State which parasite is depicted.
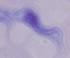

This is a trypanosome.

Summary:
  - Magnification: 1000x
  - Modality: photomicrograph